Report the malaria status of this cell.
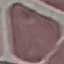
Uninfected.

image_type: automatically extracted cell patch, resized to 64 × 64 pixels
preparation: thin blood film
capture: smartphone through the microscope eyepiece
stain: Giemsa